Give the position of every Plasmodium parasite visible.
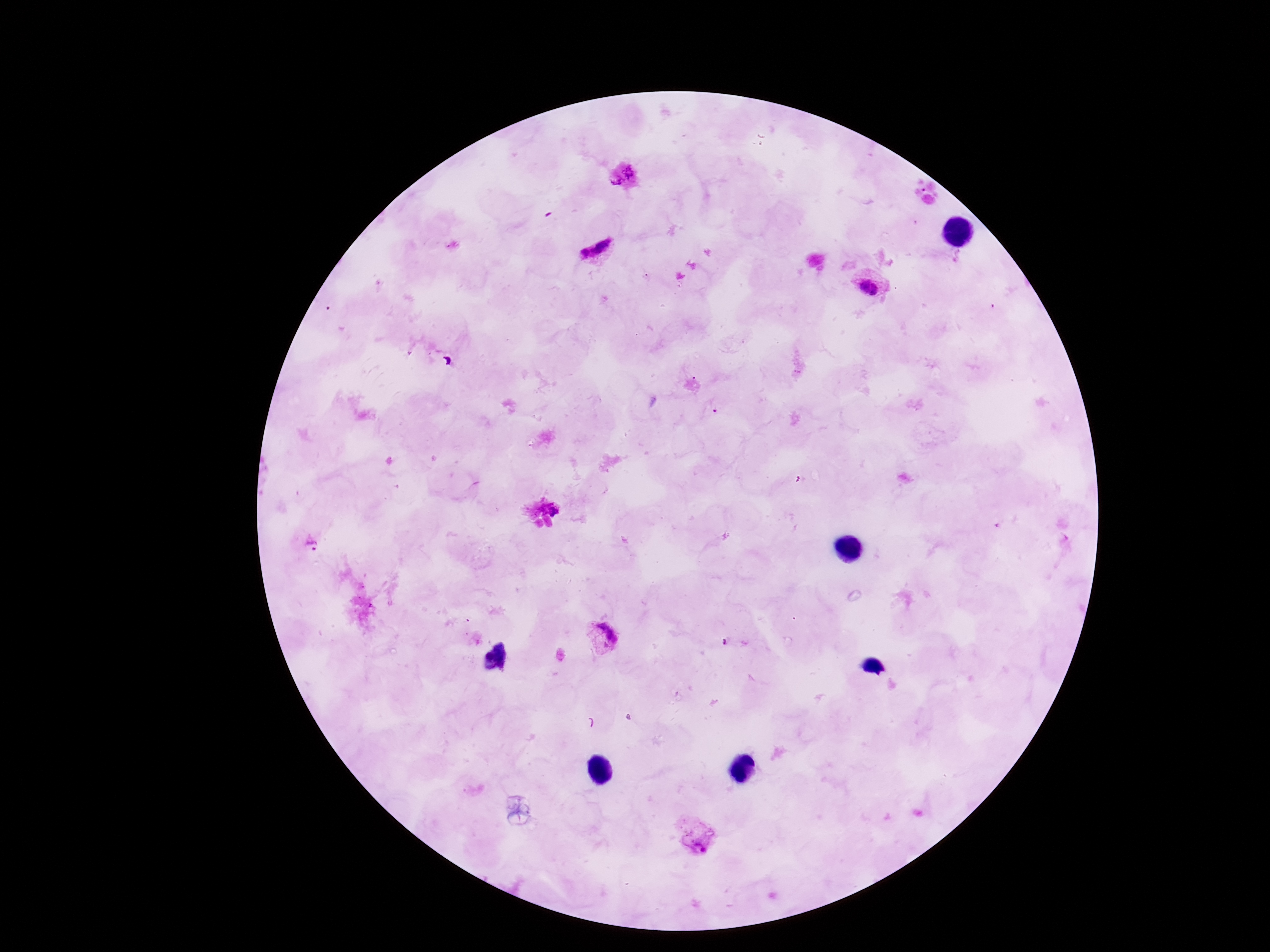

Approximate centers as [x, y] in pixels.
Plasmodium parasites: [621, 177], [595, 251], [871, 288], [311, 541], [602, 637], [695, 836].

Summary:
  - Patient malaria status: positive
  - Image size: 1270×952 pixels
  - Magnification: 100x
  - Stain: Giemsa
  - Field of view: one from this slide
  - Capture: smartphone camera through the microscope eyepiece
  - Preparation: thick peripheral-blood smear